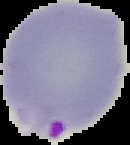

Image is 130×145 pixels. Result: Plasmodium parasites detected. The area outside the segmented cell region is set to black. From a thin blood film.